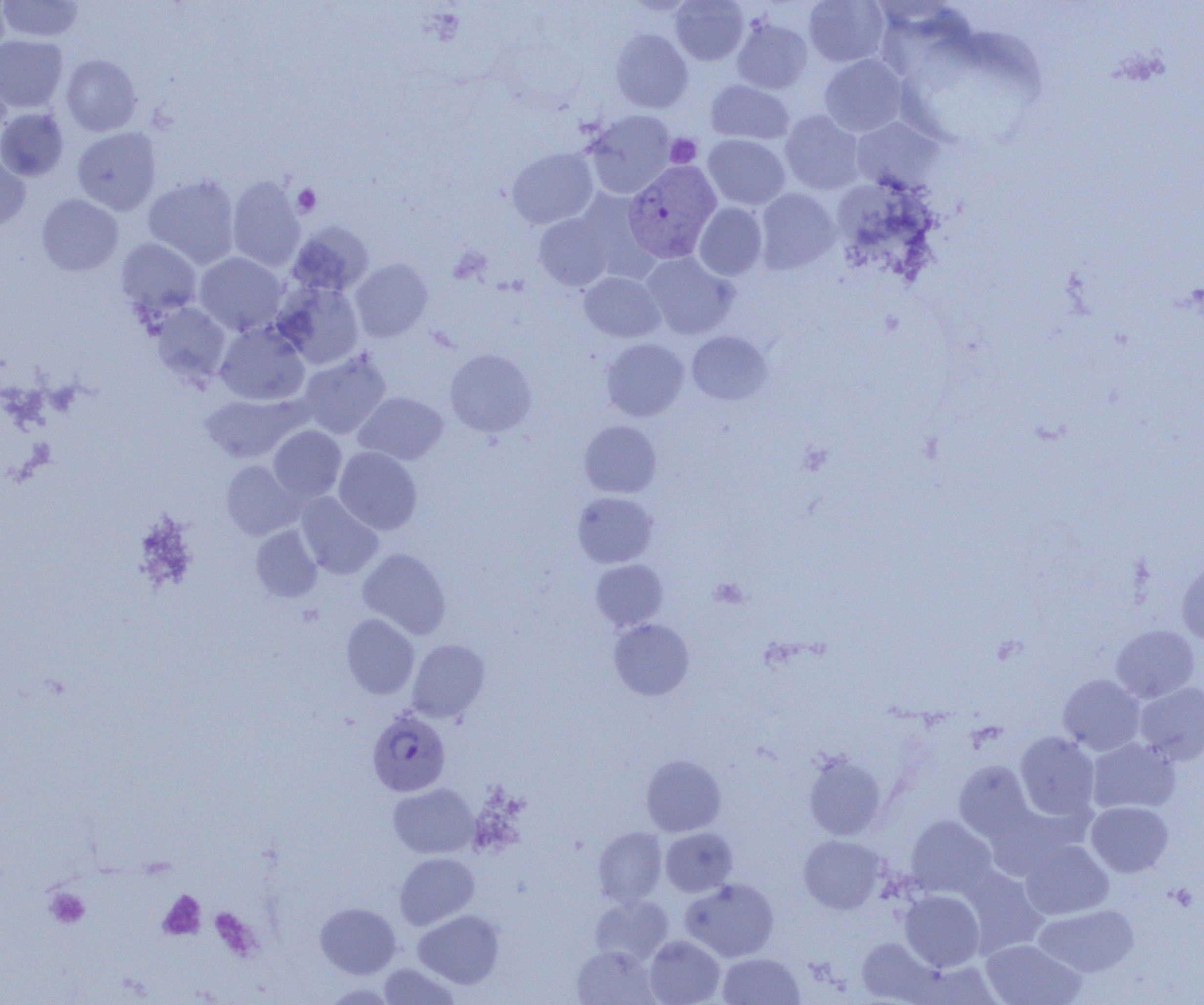
slide-level diagnosis = Plasmodium vivax
preparation = thin blood smear
image size = 1204×1005 pixels
modality = optical microscopy
Plasmodium vivax-infected red blood cell locations = approximate bounding boxes as (x1,y1)-(x2,y2) corner pairs in pixels: (624,161)-(722,264), (367,709)-(450,796)
magnification = 1000x
platelet locations = approximate bounding boxes as (x1,y1)-(x2,y2) corner pairs in pixels: (665,134)-(701,167), (292,183)-(321,216), (709,578)-(749,608), (45,887)-(90,929), (158,890)-(206,940), (209,907)-(261,961)
field of view = single
uninfected red blood cell locations = approximate bounding boxes as (x1,y1)-(x2,y2) corner pairs in pixels: (0,0)-(10,61), (0,0)-(84,42), (670,0)-(748,65), (804,0)-(889,67), (732,17)-(813,94), (610,29)-(693,113), (0,35)-(68,113), (61,54)-(141,136), (819,55)-(908,137), (0,66)-(12,141), (706,80)-(794,144), (0,108)-(68,181), (585,110)-(676,199), (780,110)-(865,195), (851,117)-(943,192), (72,127)-(161,216), (703,135)-(790,210), (507,148)-(599,228), (0,150)-(30,232), (143,174)-(240,268), (227,176)-(306,272), (755,188)-(840,273), (573,190)-(658,281), (37,194)-(123,276), (694,202)-(768,280), (533,212)-(615,291), (287,222)-(372,297), (116,238)-(202,321), (642,252)-(738,340), (195,253)-(287,337), (351,259)-(433,341), (579,272)-(665,343), (272,280)-(365,369), (151,303)-(232,385), (215,324)-(309,406), (687,331)-(772,405), (602,338)-(688,421), (445,348)-(537,437), (298,351)-(391,439), (354,392)-(447,465), (200,393)-(305,463), (579,420)-(662,498), (269,425)-(347,501), (334,447)-(422,535), (221,460)-(304,540), (572,492)-(657,568), (296,493)-(383,579), (250,525)-(322,601), (357,548)-(451,639), (591,559)-(668,632), (1177,559)-(1204,645), (341,614)-(419,699), (609,618)-(694,700), (1111,624)-(1199,703), (407,639)-(489,722), (1058,674)-(1144,755), (1135,682)-(1204,765), (1015,731)-(1099,820), (1087,737)-(1180,814), (803,751)-(887,841), (641,754)-(726,837), (954,760)-(1034,841), (388,783)-(479,859), (1086,802)-(1173,876), (906,815)-(997,898), (593,827)-(667,906), (660,827)-(738,897), (799,835)-(886,913), (1020,839)-(1113,919), (395,853)-(478,929), (958,866)-(1048,956), (681,878)-(779,962), (900,890)-(984,971), (589,895)-(672,966), (315,903)-(401,978), (1033,904)-(1138,977), (413,909)-(503,988), (644,935)-(724,1005), (857,937)-(940,1003), (980,939)-(1086,1005), (572,945)-(659,1005), (718,952)-(804,1005), (378,963)-(460,1004)